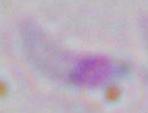

identification: Toxoplasma gondii
modality: photomicrograph
magnification: 1000x